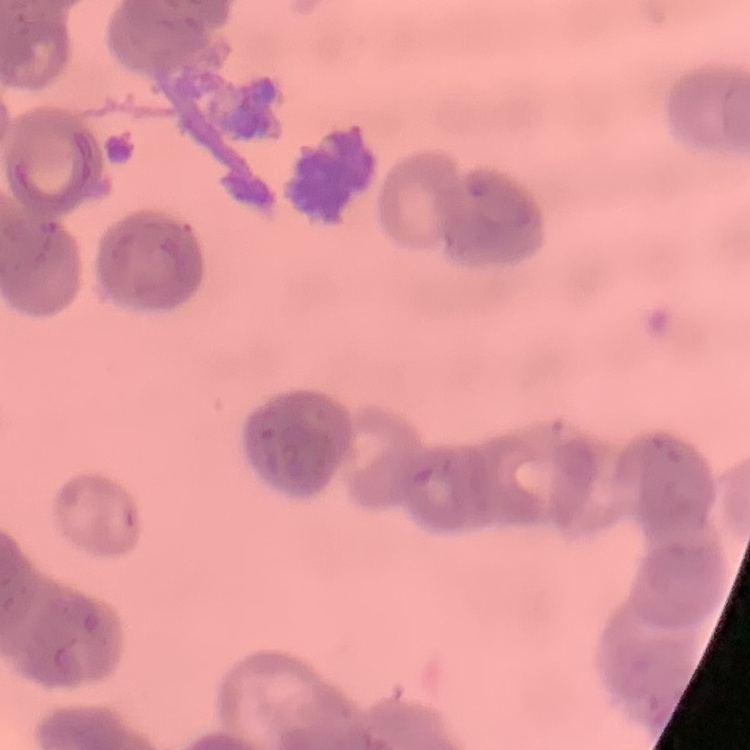

Summary:
  - Red blood cell morphology: rouleaux formation
  - Preparation: thin peripheral smear
  - Image type: one tile cut from a larger photomicrograph
  - Stain: Field's or Giemsa